Comment on the morphology of the erythrocytes.
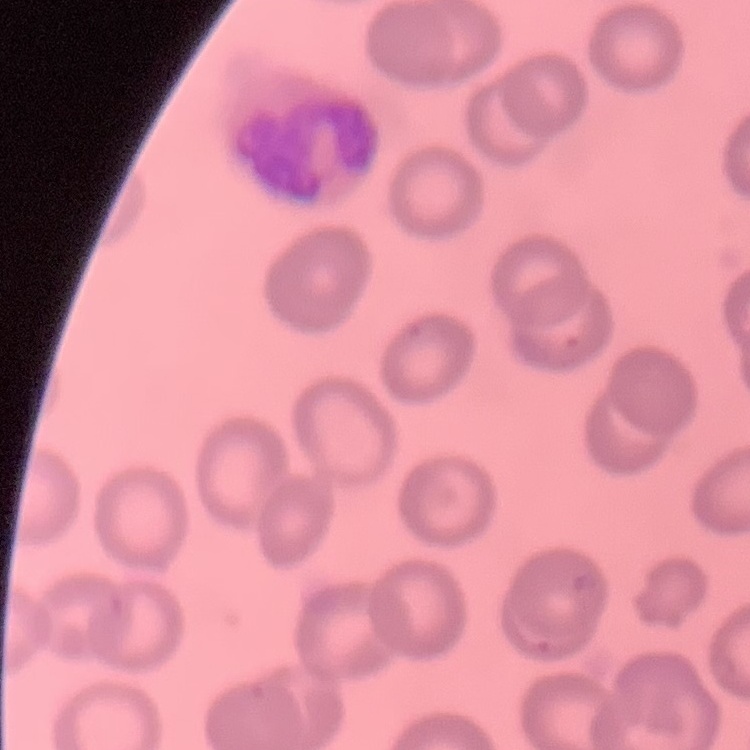
They show no rouleaux formation.

Summary:
  - Stain: Field's or Giemsa
  - Image type: one tile cut from a larger photomicrograph
  - Preparation: thin blood film